Locate every blood parasite and identify its species.
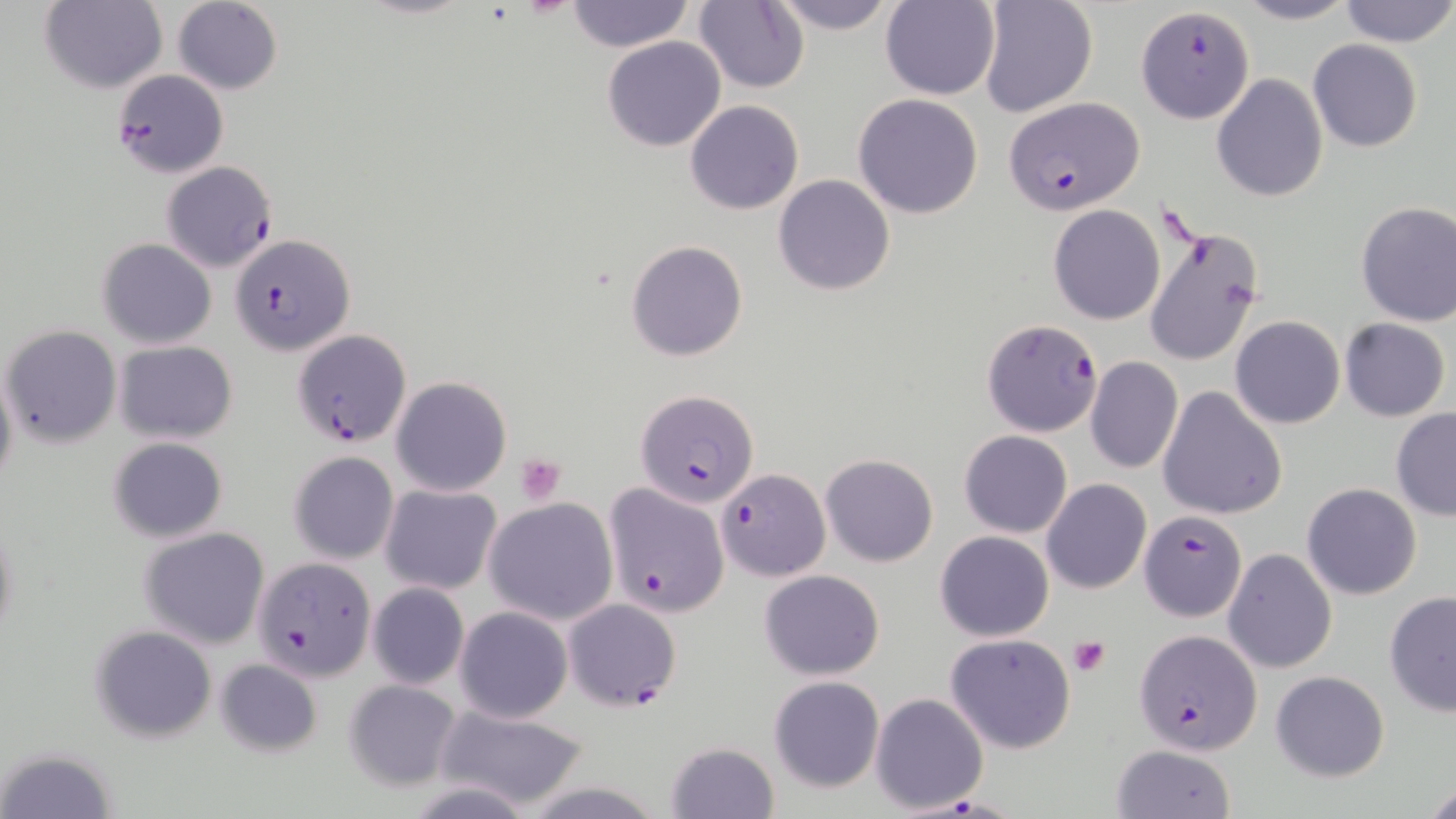

Approximate bounding boxes as (x1,y1)-(x2,y2) corner pairs in pixels.
Plasmodium falciparum-infected red blood cells: (111,69)-(229,177), (1005,95)-(1144,213), (161,161)-(278,273), (230,233)-(354,356), (981,320)-(1101,437), (292,328)-(412,449), (636,388)-(762,505), (718,468)-(827,580), (604,482)-(727,616), (1136,512)-(1246,620), (253,556)-(377,681), (561,599)-(682,712), (1135,628)-(1263,757).
No Plasmodium ovale, Plasmodium malariae, Plasmodium vivax, Babesia divergens, or Trypanosoma brucei observed.

slide-level diagnosis = Plasmodium falciparum
platelet locations = approximate bounding boxes as (x1,y1)-(x2,y2) corner pairs in pixels: (515,453)-(566,504), (1068,637)-(1110,676)
preparation = thin blood film
image size = 1456×819 pixels
uninfected red blood cell locations = approximate bounding boxes as (x1,y1)-(x2,y2) corner pairs in pixels: (172,0)-(284,95), (565,0)-(692,53), (767,0)-(902,33), (880,0)-(1000,100), (1234,0)-(1359,25), (1338,0)-(1456,48), (41,1)-(167,93), (694,1)-(809,92), (977,1)-(1097,118), (1136,5)-(1255,124), (602,36)-(725,151), (1307,39)-(1424,152), (1211,74)-(1327,203), (852,93)-(984,219), (685,99)-(803,215), (773,174)-(895,295), (1355,201)-(1456,327), (1049,204)-(1165,324), (1144,220)-(1265,366), (98,237)-(216,348), (626,240)-(748,362), (1230,315)-(1345,428), (1340,318)-(1450,421), (3,325)-(121,446), (114,341)-(238,443), (1084,356)-(1182,473), (0,360)-(18,494), (392,377)-(511,496), (1159,387)-(1288,520), (1390,407)-(1456,521), (960,429)-(1072,537), (108,436)-(228,543), (288,452)-(398,564), (820,454)-(939,568), (1041,478)-(1152,594), (1303,482)-(1421,600), (380,484)-(502,595), (485,497)-(619,625), (1,514)-(19,653), (139,528)-(270,649), (935,530)-(1053,641), (1223,548)-(1337,672), (759,569)-(884,679), (367,583)-(469,690), (1384,590)-(1456,716), (454,607)-(574,723), (89,624)-(218,741), (944,633)-(1077,753), (215,658)-(323,757), (1271,671)-(1390,781), (769,676)-(885,792), (342,679)-(461,792), (870,692)-(989,814), (434,704)-(591,811), (665,742)-(779,818), (1112,744)-(1237,819), (3,747)-(118,819), (1423,782)-(1456,818)
magnification = 1000x
modality = optical microscopy
stain = May-Grünwald-Giemsa
field of view = one of a larger specimen